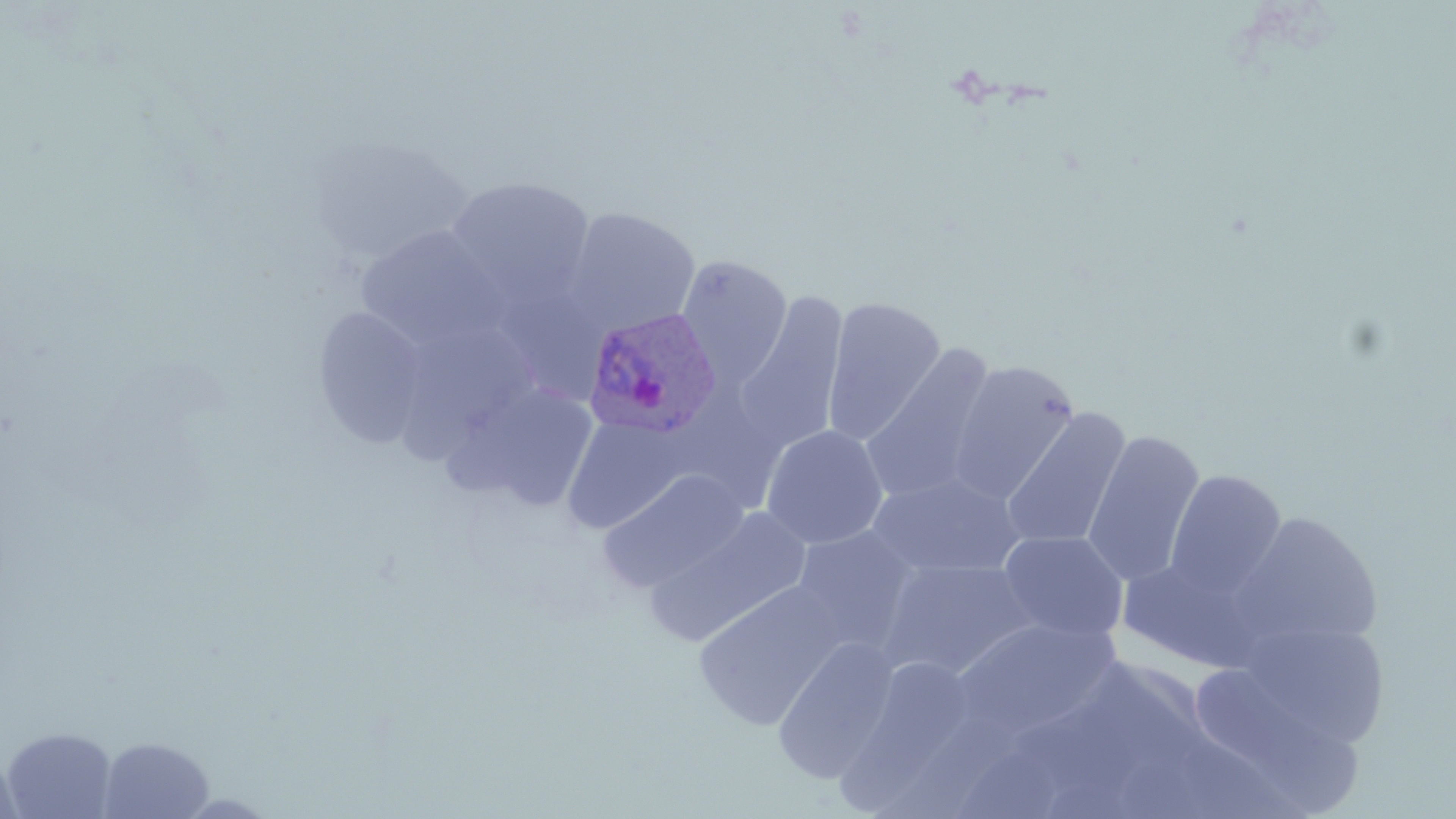

Approximate bounding boxes as named x1/y1/x2/y2 corners in pixels. Plasmodium ovale-infected red blood cell locations: (x1=581, y1=306, x2=723, y2=440). Uninfected red blood cell locations: (x1=444, y1=176, x2=596, y2=310), (x1=565, y1=206, x2=700, y2=334), (x1=355, y1=225, x2=505, y2=352), (x1=675, y1=255, x2=793, y2=385), (x1=500, y1=281, x2=621, y2=403), (x1=735, y1=291, x2=849, y2=453), (x1=822, y1=297, x2=946, y2=444), (x1=312, y1=306, x2=432, y2=448), (x1=406, y1=318, x2=540, y2=469), (x1=860, y1=343, x2=999, y2=505), (x1=946, y1=359, x2=1081, y2=503), (x1=450, y1=379, x2=600, y2=512), (x1=1000, y1=408, x2=1131, y2=551), (x1=561, y1=415, x2=691, y2=534), (x1=760, y1=424, x2=888, y2=549), (x1=1082, y1=430, x2=1205, y2=587), (x1=598, y1=469, x2=750, y2=593), (x1=1164, y1=470, x2=1287, y2=598), (x1=867, y1=474, x2=1027, y2=579), (x1=644, y1=507, x2=813, y2=647), (x1=1231, y1=511, x2=1382, y2=652), (x1=790, y1=524, x2=924, y2=654), (x1=997, y1=529, x2=1129, y2=643), (x1=1118, y1=552, x2=1272, y2=673), (x1=878, y1=559, x2=1040, y2=680), (x1=692, y1=581, x2=847, y2=731), (x1=1223, y1=617, x2=1397, y2=756), (x1=947, y1=618, x2=1124, y2=747), (x1=771, y1=637, x2=901, y2=783), (x1=1196, y1=660, x2=1359, y2=818), (x1=828, y1=668, x2=975, y2=819), (x1=2, y1=727, x2=117, y2=818), (x1=98, y1=735, x2=215, y2=818), (x1=957, y1=747, x2=1072, y2=819), (x1=0, y1=751, x2=26, y2=819), (x1=174, y1=792, x2=282, y2=817). Slide-level diagnosis: Plasmodium ovale. May-Grünwald-Giemsa-stained preparation. Thin blood film. One field of a larger specimen. Image is 1456×819 pixels. Optical microscopy. 1000x magnification.